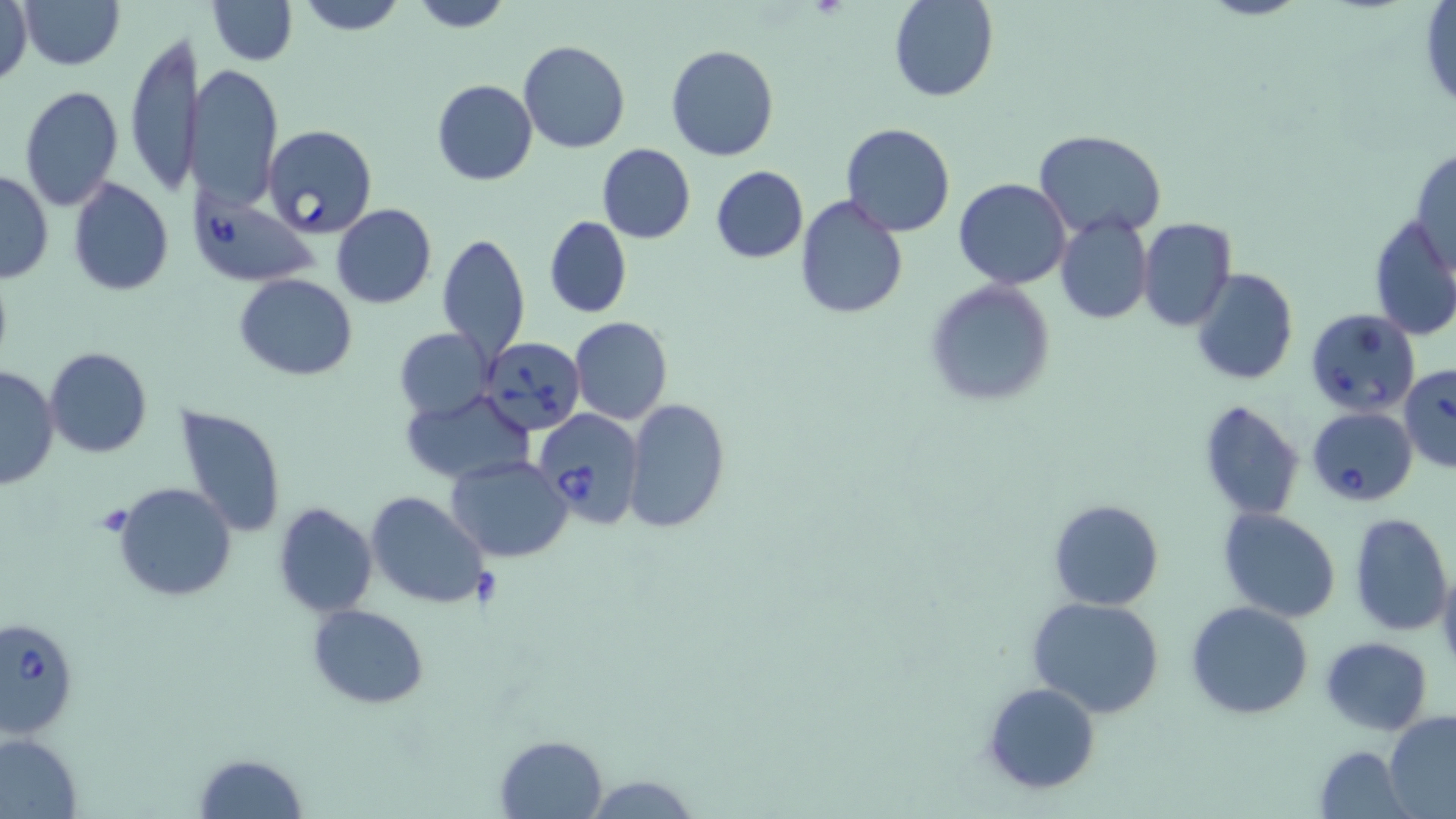 Approximate bounding boxes as named x1/y1/x2/y2 corners in pixels. Uninfected red blood cell locations: (x1=1, y1=0, x2=33, y2=89), (x1=18, y1=0, x2=124, y2=70), (x1=206, y1=0, x2=298, y2=66), (x1=294, y1=0, x2=409, y2=35), (x1=407, y1=0, x2=513, y2=31), (x1=888, y1=0, x2=998, y2=102), (x1=1418, y1=2, x2=1456, y2=111), (x1=124, y1=31, x2=199, y2=197), (x1=519, y1=39, x2=630, y2=154), (x1=665, y1=44, x2=780, y2=162), (x1=188, y1=62, x2=283, y2=211), (x1=432, y1=80, x2=538, y2=186), (x1=20, y1=83, x2=122, y2=213), (x1=840, y1=121, x2=955, y2=238), (x1=1035, y1=130, x2=1165, y2=236), (x1=597, y1=143, x2=695, y2=244), (x1=1410, y1=148, x2=1456, y2=272), (x1=711, y1=165, x2=808, y2=263), (x1=0, y1=168, x2=53, y2=283), (x1=67, y1=177, x2=174, y2=295), (x1=954, y1=178, x2=1071, y2=290), (x1=795, y1=193, x2=908, y2=318), (x1=331, y1=203, x2=438, y2=309), (x1=1054, y1=214, x2=1152, y2=325), (x1=1369, y1=214, x2=1456, y2=342), (x1=545, y1=216, x2=632, y2=318), (x1=1137, y1=217, x2=1237, y2=331), (x1=436, y1=230, x2=530, y2=363), (x1=1191, y1=267, x2=1298, y2=386), (x1=235, y1=274, x2=356, y2=380), (x1=924, y1=279, x2=1057, y2=410), (x1=570, y1=316, x2=673, y2=423), (x1=395, y1=328, x2=493, y2=421), (x1=44, y1=346, x2=153, y2=459), (x1=0, y1=366, x2=59, y2=489), (x1=401, y1=389, x2=536, y2=486), (x1=621, y1=398, x2=730, y2=532), (x1=1198, y1=398, x2=1304, y2=521), (x1=177, y1=404, x2=287, y2=538), (x1=448, y1=455, x2=572, y2=561), (x1=114, y1=482, x2=238, y2=603), (x1=365, y1=491, x2=488, y2=608), (x1=1048, y1=499, x2=1164, y2=609), (x1=272, y1=503, x2=377, y2=617), (x1=1219, y1=509, x2=1342, y2=623), (x1=1350, y1=514, x2=1453, y2=636), (x1=1437, y1=565, x2=1456, y2=672), (x1=1027, y1=597, x2=1167, y2=719), (x1=1185, y1=600, x2=1314, y2=719), (x1=308, y1=604, x2=430, y2=708), (x1=1320, y1=636, x2=1433, y2=734), (x1=981, y1=681, x2=1101, y2=795), (x1=1384, y1=711, x2=1456, y2=816), (x1=0, y1=732, x2=82, y2=817), (x1=494, y1=735, x2=609, y2=819), (x1=1313, y1=743, x2=1413, y2=818), (x1=193, y1=752, x2=307, y2=818), (x1=579, y1=774, x2=704, y2=817). Babesia divergens-infected red blood cell locations: (x1=262, y1=124, x2=377, y2=239), (x1=188, y1=189, x2=318, y2=287), (x1=1305, y1=308, x2=1419, y2=418), (x1=481, y1=337, x2=586, y2=436), (x1=1398, y1=365, x2=1456, y2=473), (x1=1305, y1=405, x2=1420, y2=507), (x1=533, y1=409, x2=643, y2=528), (x1=1, y1=614, x2=78, y2=739). Slide-level diagnosis: Babesia divergens. Optical microscopy. Image is 1456×819 pixels. May-Grünwald-Giemsa stain. 1000x magnification. Single field of view. Thin blood smear.